Classify this cell by malaria status.
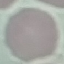

Uninfected.

Thin blood film. Giemsa stain. Automatically extracted cell patch, resized to 64 × 64 pixels. Acquired by smartphone through the microscope eyepiece.